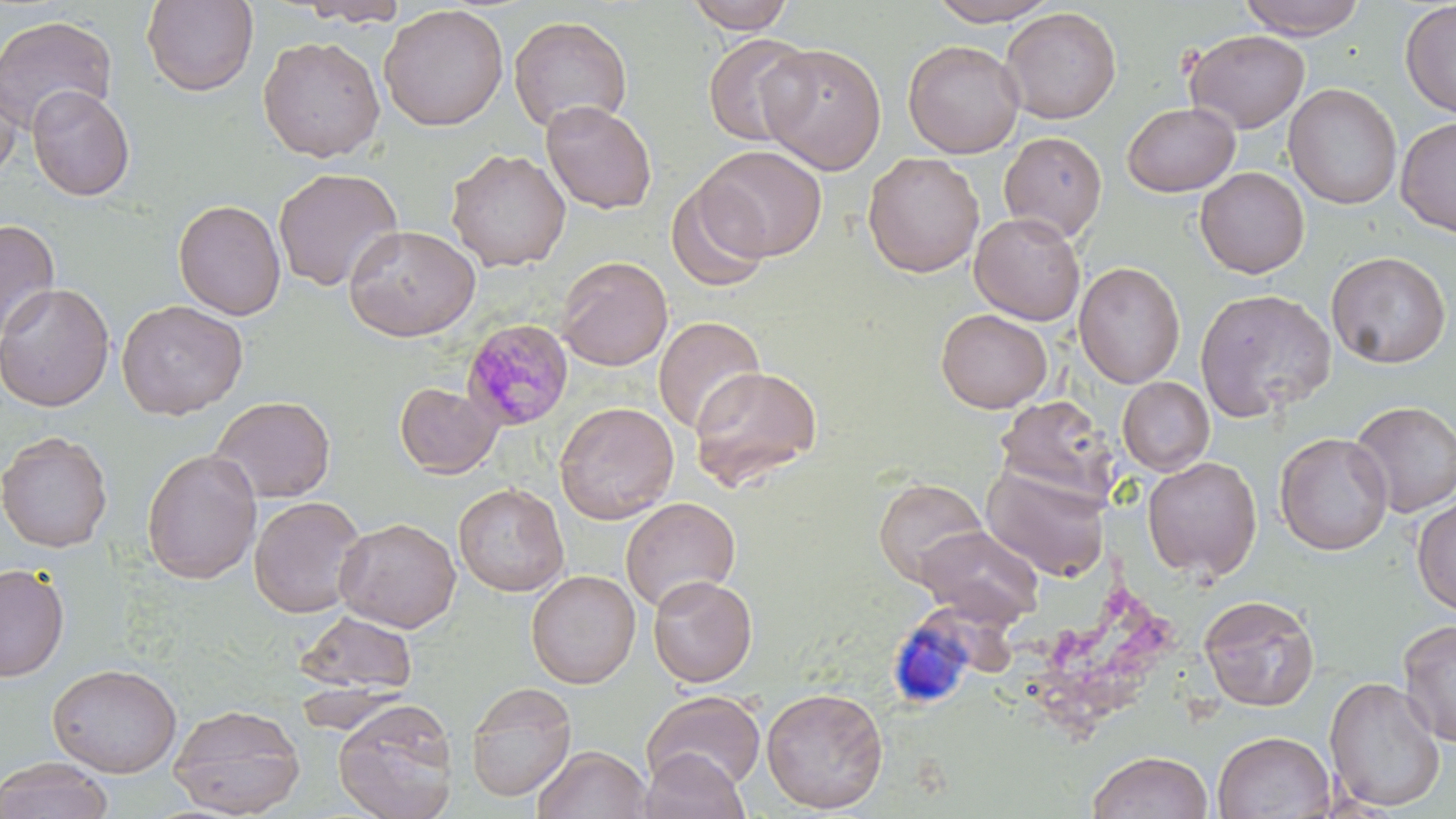

Summary:
  - Coordinate format: approximate bounding boxes as (x1, y1, x2, y2) in pixels
  - Plasmodium malariae-infected red blood cell locations: (462, 318, 575, 432)
  - Uninfected red blood cell locations: (297, 0, 408, 27), (684, 0, 796, 34), (925, 0, 1060, 26), (1236, 0, 1369, 40), (141, 1, 259, 96), (1399, 1, 1456, 118), (379, 4, 509, 131), (1000, 7, 1122, 124), (0, 14, 118, 135), (508, 15, 632, 133), (1183, 29, 1310, 133), (703, 32, 814, 147), (258, 35, 385, 163), (902, 40, 1024, 158), (758, 42, 887, 174), (0, 71, 22, 181), (1283, 83, 1402, 210), (26, 84, 136, 201), (541, 99, 657, 214), (1121, 102, 1240, 197), (1395, 116, 1456, 237), (999, 131, 1108, 242), (698, 145, 827, 261), (445, 148, 571, 272), (863, 152, 984, 277), (272, 167, 404, 293), (1194, 167, 1310, 279), (664, 178, 772, 293), (173, 199, 287, 320), (970, 212, 1085, 325), (0, 218, 60, 343), (344, 224, 481, 342), (1326, 251, 1451, 369), (556, 255, 673, 371), (1074, 262, 1186, 388), (0, 282, 115, 412), (1195, 288, 1337, 422), (116, 299, 248, 419), (936, 308, 1052, 413), (653, 316, 766, 435), (688, 365, 823, 490), (1117, 377, 1215, 476), (393, 381, 503, 479), (210, 396, 336, 503), (996, 396, 1115, 500), (555, 401, 679, 524), (1349, 401, 1456, 518), (0, 431, 113, 553), (1274, 432, 1393, 556), (141, 448, 262, 585), (1142, 456, 1262, 580), (981, 460, 1112, 581), (873, 477, 989, 587), (453, 482, 569, 596), (249, 496, 367, 618), (1411, 496, 1456, 617), (620, 497, 741, 613), (334, 517, 461, 632), (916, 524, 1045, 626), (0, 563, 70, 682), (526, 569, 641, 689), (648, 574, 758, 688), (1199, 593, 1321, 711), (294, 609, 418, 695), (1397, 618, 1456, 746), (47, 663, 182, 778), (1324, 676, 1446, 813), (466, 681, 577, 802), (761, 686, 889, 813), (641, 689, 766, 793), (333, 698, 459, 819), (168, 703, 304, 818), (1213, 731, 1335, 818), (533, 745, 652, 819), (641, 748, 750, 819), (1088, 749, 1213, 819), (0, 756, 113, 819)
  - Slide-level diagnosis: Plasmodium malariae
  - Preparation: thin blood smear
  - Magnification: 1000x
  - Field of view: one of a larger specimen
  - Modality: optical microscopy
  - Stain: May-Grünwald-Giemsa
  - Image size: 1456×819 pixels